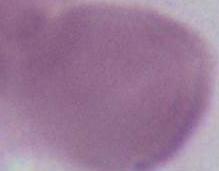
magnification = 1000x
identification = erythrocyte
modality = micrograph